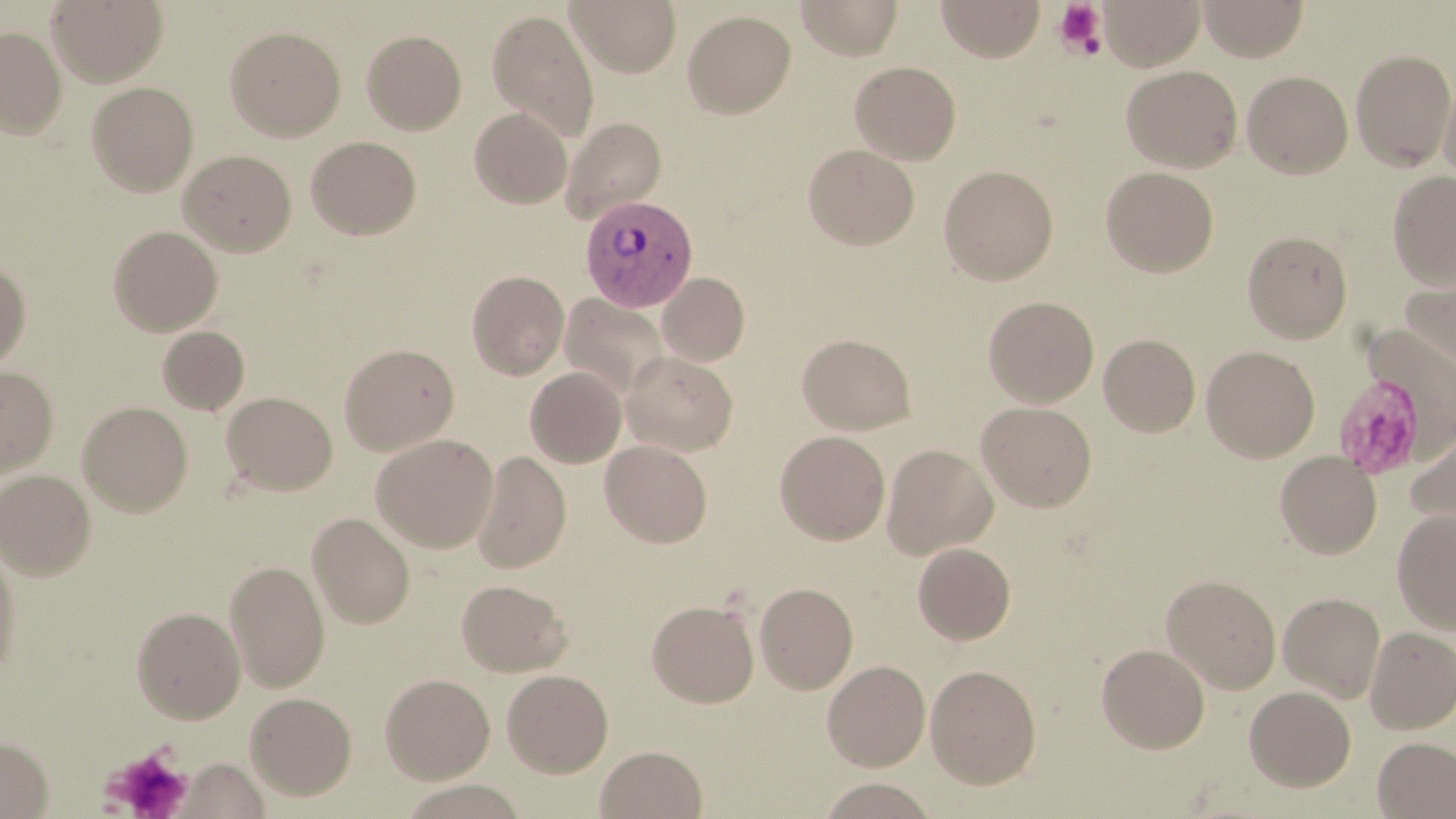
Approximate bounding boxes as named x1/y1/x2/y2 corners in pixels. Platelet locations: (x1=1053, y1=2, x2=1107, y2=58), (x1=1333, y1=371, x2=1431, y2=481), (x1=103, y1=745, x2=193, y2=819). Plasmodium vivax-infected red blood cell locations: (x1=580, y1=195, x2=697, y2=312). Uninfected red blood cell locations: (x1=46, y1=0, x2=168, y2=86), (x1=567, y1=0, x2=681, y2=77), (x1=796, y1=0, x2=904, y2=60), (x1=935, y1=0, x2=1045, y2=62), (x1=1099, y1=0, x2=1205, y2=70), (x1=1198, y1=0, x2=1309, y2=61), (x1=486, y1=8, x2=599, y2=142), (x1=682, y1=9, x2=796, y2=119), (x1=225, y1=25, x2=346, y2=141), (x1=0, y1=26, x2=67, y2=138), (x1=361, y1=29, x2=467, y2=135), (x1=1351, y1=49, x2=1455, y2=171), (x1=849, y1=61, x2=961, y2=164), (x1=1121, y1=65, x2=1243, y2=172), (x1=1242, y1=70, x2=1353, y2=178), (x1=1440, y1=73, x2=1456, y2=189), (x1=86, y1=81, x2=199, y2=197), (x1=469, y1=108, x2=572, y2=207), (x1=561, y1=117, x2=667, y2=222), (x1=306, y1=136, x2=421, y2=239), (x1=803, y1=144, x2=919, y2=250), (x1=178, y1=149, x2=296, y2=256), (x1=939, y1=164, x2=1059, y2=284), (x1=1100, y1=166, x2=1219, y2=277), (x1=1388, y1=170, x2=1456, y2=288), (x1=108, y1=225, x2=223, y2=336), (x1=1242, y1=229, x2=1353, y2=343), (x1=0, y1=260, x2=31, y2=373), (x1=1400, y1=266, x2=1456, y2=373), (x1=466, y1=270, x2=569, y2=379), (x1=658, y1=273, x2=749, y2=366), (x1=561, y1=294, x2=669, y2=398), (x1=983, y1=295, x2=1099, y2=407), (x1=157, y1=325, x2=249, y2=415), (x1=797, y1=333, x2=916, y2=434), (x1=1099, y1=333, x2=1201, y2=436), (x1=339, y1=343, x2=459, y2=455), (x1=1202, y1=345, x2=1320, y2=462), (x1=622, y1=351, x2=737, y2=455), (x1=0, y1=366, x2=58, y2=479), (x1=525, y1=367, x2=627, y2=467), (x1=222, y1=391, x2=337, y2=495), (x1=77, y1=400, x2=194, y2=516), (x1=975, y1=401, x2=1097, y2=512), (x1=1404, y1=421, x2=1456, y2=543), (x1=775, y1=430, x2=890, y2=544), (x1=371, y1=433, x2=498, y2=552), (x1=600, y1=439, x2=713, y2=547), (x1=882, y1=444, x2=997, y2=558), (x1=1275, y1=451, x2=1382, y2=558), (x1=471, y1=452, x2=571, y2=575), (x1=0, y1=469, x2=96, y2=580), (x1=1392, y1=509, x2=1456, y2=634), (x1=307, y1=512, x2=415, y2=629), (x1=0, y1=538, x2=23, y2=680), (x1=913, y1=542, x2=1016, y2=644), (x1=225, y1=559, x2=330, y2=692), (x1=1161, y1=573, x2=1282, y2=694), (x1=456, y1=579, x2=572, y2=676), (x1=755, y1=582, x2=858, y2=694), (x1=1278, y1=591, x2=1385, y2=702), (x1=647, y1=599, x2=759, y2=708), (x1=131, y1=606, x2=246, y2=723), (x1=1365, y1=627, x2=1456, y2=734), (x1=1096, y1=643, x2=1210, y2=753), (x1=822, y1=660, x2=930, y2=771), (x1=925, y1=663, x2=1042, y2=789), (x1=502, y1=669, x2=613, y2=777), (x1=380, y1=673, x2=495, y2=783), (x1=1244, y1=685, x2=1356, y2=791), (x1=245, y1=692, x2=356, y2=799), (x1=0, y1=735, x2=53, y2=818), (x1=1373, y1=736, x2=1456, y2=818), (x1=596, y1=745, x2=707, y2=818). Slide-level diagnosis: Plasmodium vivax. Thin blood smear. Image is 1456×819 pixels. Captured at 1000x magnification. Optical microscopy. May-Grünwald-Giemsa stain. Single field of view.